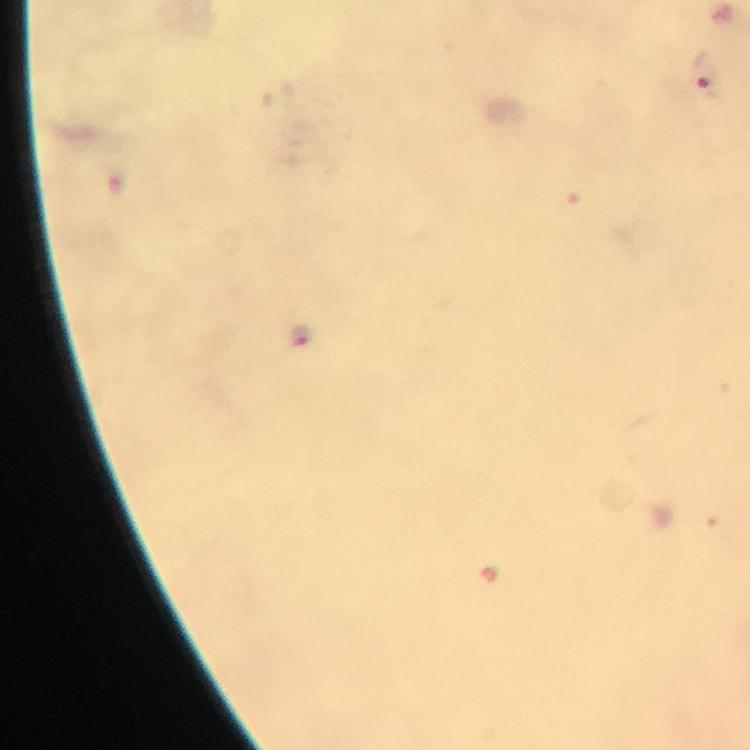
capture: smartphone photograph through a microscope
magnification: 100x
image_size: 750×750 pixels
context: from a malaria diagnostic workup
stain: Giemsa
cropped_from: a single field of view
preparation: thick blood film
immersion_oil: applied
plasmodium_parasite_locations: 'approximate centers as {x, y} in pixels: {705, 75}, {302, 337}'